Give a bounding box for every leukocyte visible.
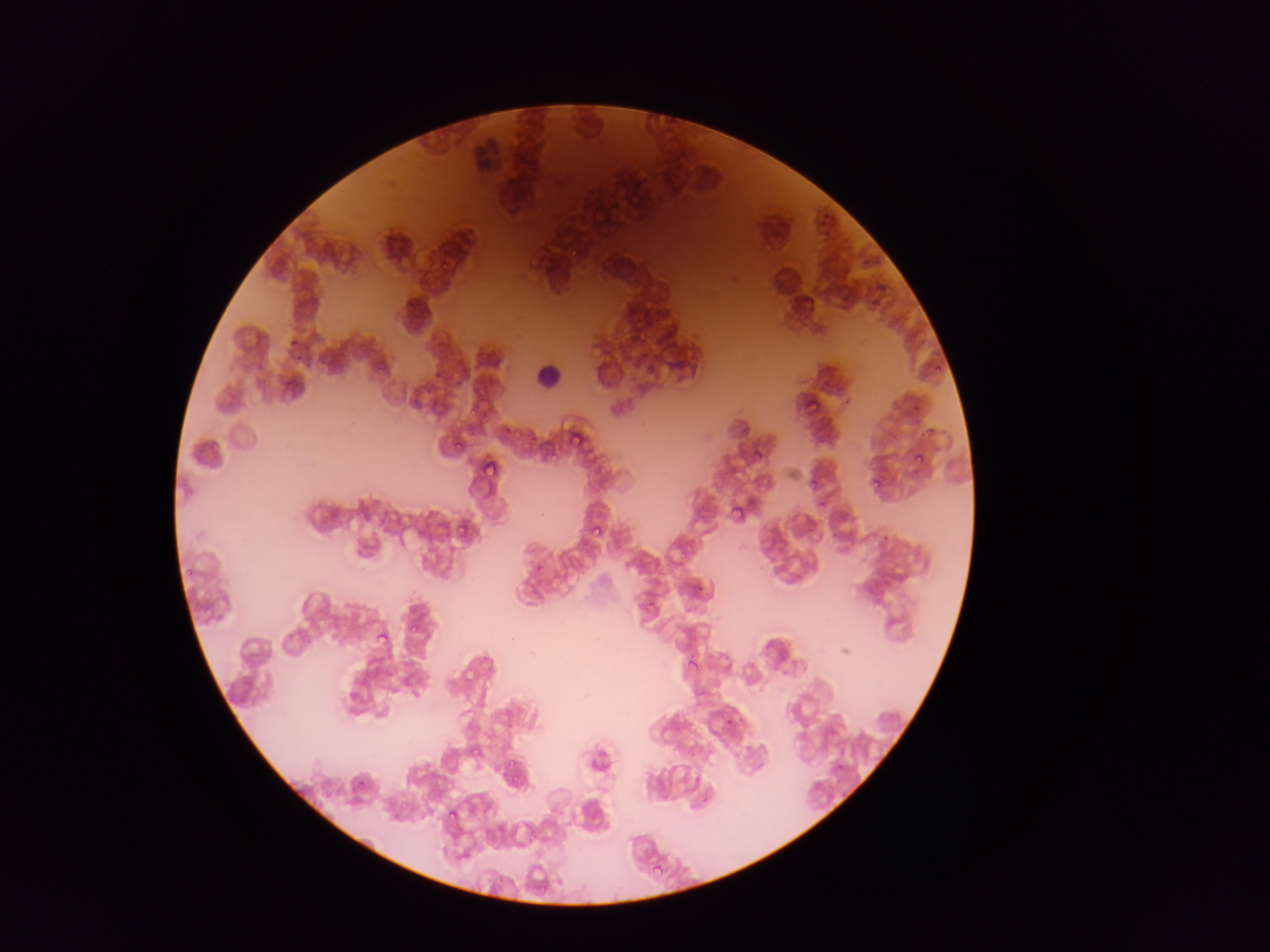

Approximate bounding boxes as [left, top, right, bottom] in pixels.
Leukocytes: [526, 345, 579, 414].

Malaria parasite locations: [564, 244, 580, 264], [435, 254, 457, 270], [283, 334, 298, 345], [933, 362, 944, 375], [280, 375, 295, 390], [465, 395, 481, 422], [801, 399, 820, 416], [568, 435, 583, 448], [452, 439, 467, 457], [754, 449, 763, 459], [907, 451, 923, 466], [482, 453, 506, 479], [547, 454, 560, 467], [869, 469, 889, 490], [809, 478, 818, 489], [722, 495, 749, 530], [817, 497, 830, 511], [456, 505, 470, 537], [590, 524, 602, 540], [645, 597, 661, 615], [401, 622, 428, 639], [377, 633, 390, 647], [686, 656, 702, 672], [347, 690, 361, 704], [723, 715, 737, 729], [501, 724, 514, 734], [468, 748, 485, 763], [503, 761, 523, 781], [353, 775, 368, 794], [390, 798, 409, 812], [448, 804, 460, 826], [390, 818, 396, 831], [648, 864, 662, 880]. Collected in Ghana. Thin blood smear. Image is 1270×952 pixels. Single field of view. Photographed through a microscope with a mobile-phone camera.